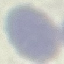

result: no malaria parasites detected
stain: Giemsa
capture: smartphone through the microscope eyepiece
image_type: automatically extracted cell patch, resized to 64 × 64 pixels
preparation: thin blood film